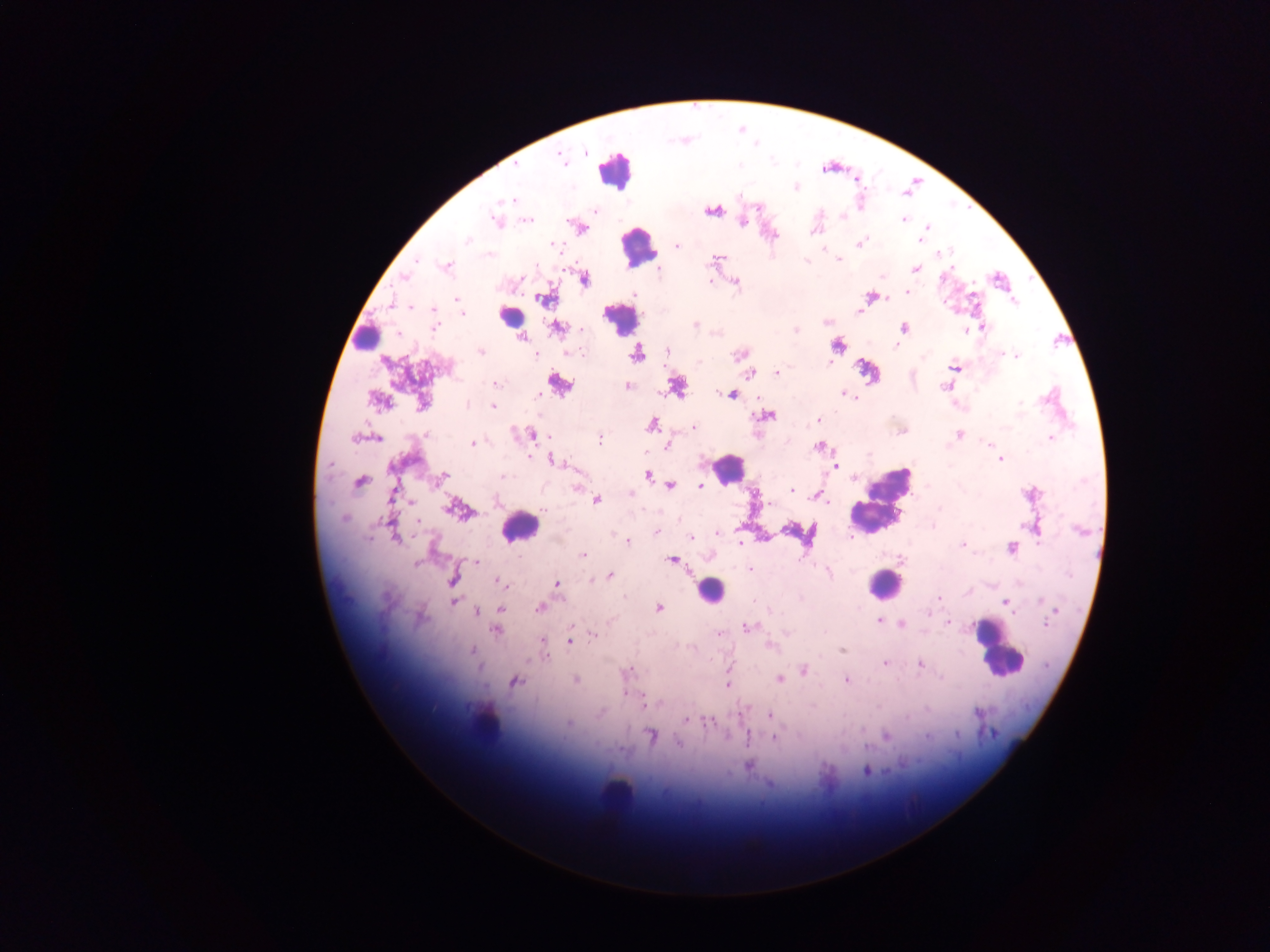
Approximate centers as {x, y} in pixels. Leukocyte locations: {614, 170}, {637, 247}, {508, 316}, {620, 318}, {365, 337}, {727, 468}, {881, 501}, {519, 526}, {884, 584}, {709, 591}, {1000, 650}, {484, 720}, {616, 790}. Plasmodium parasite locations: {584, 152}, {559, 156}, {795, 186}, {511, 199}, {595, 210}, {712, 210}, {528, 219}, {903, 219}, {742, 221}, {496, 222}, {926, 226}, {578, 227}, {924, 235}, {920, 239}, {860, 243}, {678, 247}, {716, 259}, {838, 259}, {446, 265}, {657, 268}, {916, 268}, {583, 279}, {709, 281}, {734, 282}, {907, 291}, {871, 296}, {543, 297}, {457, 298}, {860, 311}, {695, 324}, {434, 326}, {903, 327}, {982, 327}, {556, 328}, {795, 328}, {964, 328}, {520, 337}, {837, 344}, {667, 350}, {480, 351}, {567, 351}, {636, 353}, {741, 353}, {535, 354}, {1015, 355}, {954, 367}, {867, 370}, {776, 373}, {751, 374}, {559, 382}, {496, 383}, {628, 385}, {676, 385}, {946, 386}, {844, 393}, {732, 394}, {536, 396}, {378, 400}, {423, 403}, {493, 406}, {765, 415}, {818, 420}, {652, 424}, {693, 427}, {531, 434}, {958, 434}, {362, 437}, {1050, 438}, {598, 440}, {472, 443}, {667, 444}, {820, 446}, {1000, 458}, {553, 460}, {835, 464}, {647, 474}, {441, 478}, {360, 481}, {576, 486}, {670, 486}, {700, 486}, {791, 489}, {1031, 493}, {631, 494}, {817, 494}, {596, 499}, {456, 508}, {1035, 526}, {656, 532}, {717, 533}, {393, 534}, {809, 534}, {690, 537}, {627, 540}, {740, 543}, {963, 544}, {1011, 547}, {583, 555}, {901, 558}, {672, 559}, {475, 562}, {750, 568}, {828, 570}, {609, 575}, {453, 578}, {502, 583}, {556, 583}, {939, 598}, {454, 601}, {1005, 602}, {658, 607}, {500, 608}, {539, 608}, {477, 612}, {928, 612}, {879, 621}, {948, 622}, {902, 624}, {747, 627}, {496, 629}, {718, 632}, {593, 635}, {569, 640}, {542, 641}, {768, 645}, {842, 649}, {472, 650}, {544, 653}, {884, 663}, {919, 663}, {804, 669}, {628, 672}, {574, 679}, {780, 679}, {846, 680}, {515, 681}, {728, 684}, {642, 702}, {769, 715}, {686, 720}, {712, 722}, {652, 736}, {885, 736}, {773, 737}, {903, 764}, {748, 765}, {867, 771}, {769, 783}. Single field of view. Image is 1270×952 pixels. Sample from Ghana. Photographed through a microscope with a mobile-phone camera. Thick blood smear.